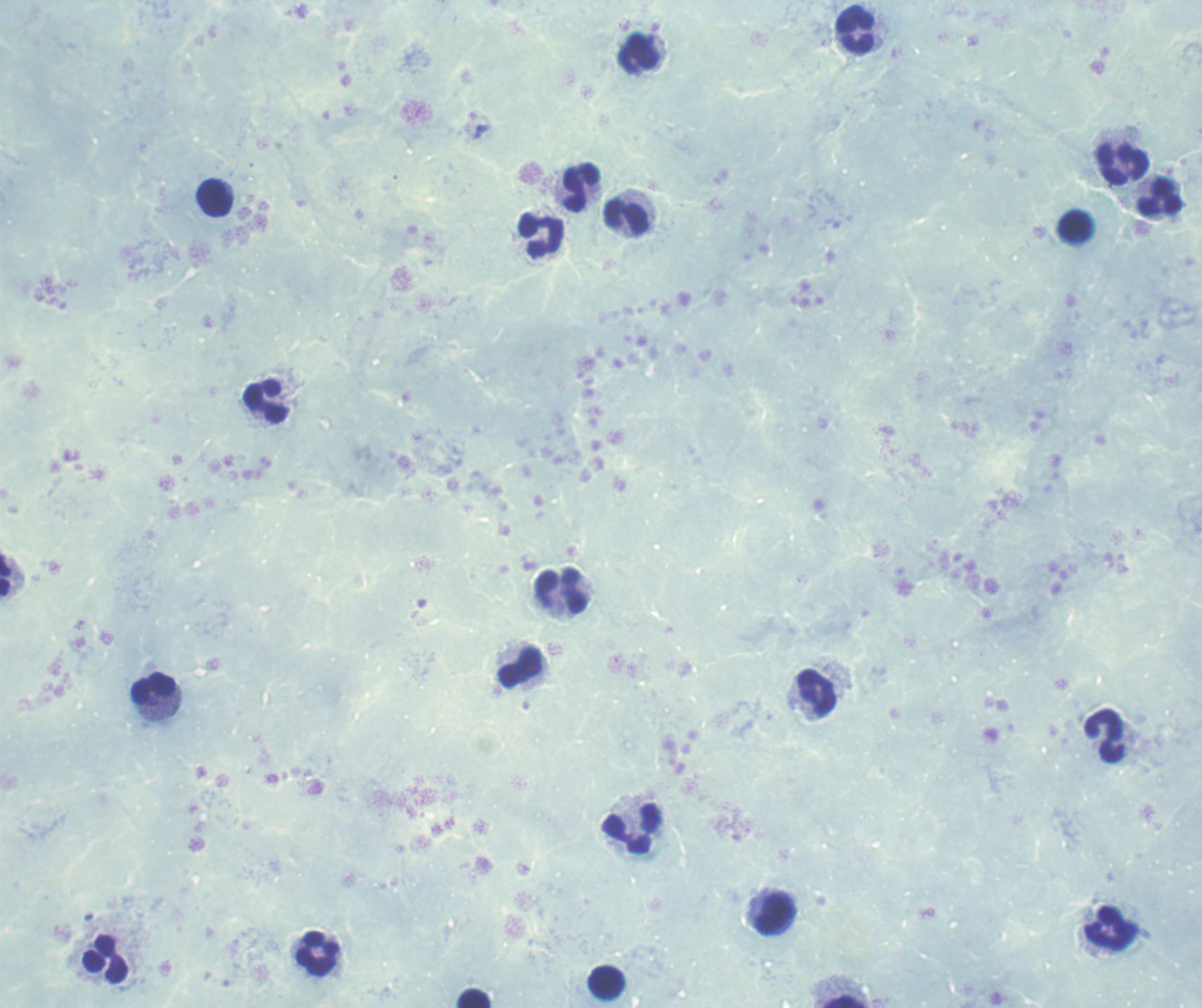
Approximate object centers, in pixels from the top-left corner. Trophozoite locations: (x=481, y=132). Leukocyte locations: (x=855, y=32), (x=638, y=54), (x=1124, y=164), (x=580, y=188), (x=214, y=197), (x=1160, y=197), (x=625, y=218), (x=1075, y=226), (x=542, y=235), (x=267, y=402), (x=5, y=577), (x=561, y=592), (x=520, y=667), (x=153, y=687), (x=817, y=694), (x=1104, y=737), (x=631, y=828), (x=774, y=913), (x=1111, y=927), (x=317, y=953), (x=105, y=960), (x=606, y=984), (x=472, y=998), (x=844, y=1002). Romanowsky stain. Background quality: poor. Thick smear of blood. Result: Plasmodium parasites detected. Previously used in a real diagnosis. Image is 1202×1008 pixels. Captured at 100x magnification. One field from this slide.